Outline each blood parasite and name the species.
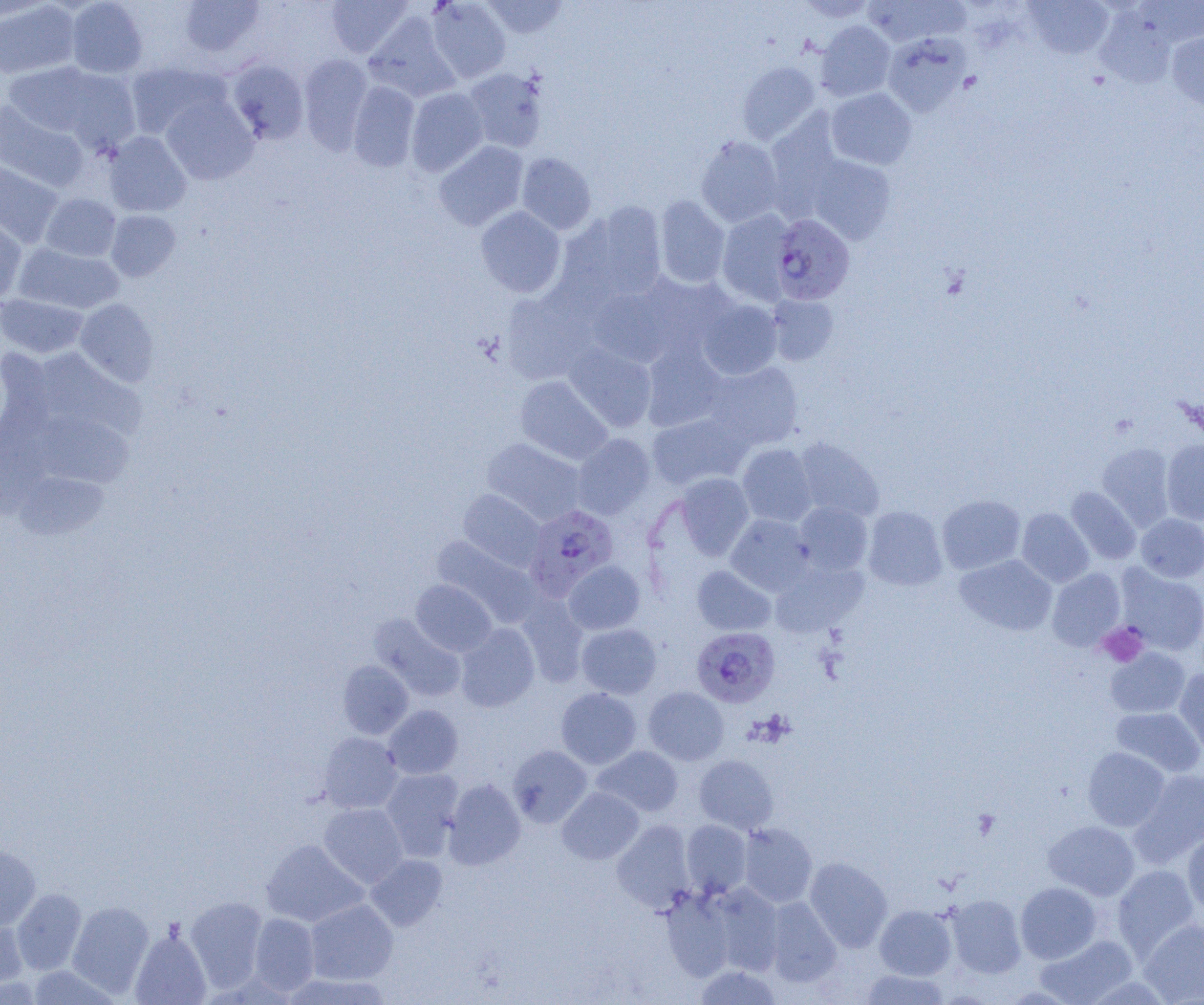
Approximate bounding boxes as (x1, y1, x2, y2) in pixels.
Plasmodium falciparum-infected red blood cells: (771, 213, 855, 304), (524, 504, 619, 600), (691, 627, 780, 708).
No Plasmodium ovale, Plasmodium malariae, Plasmodium vivax, Babesia divergens, or Trypanosoma brucei observed.

Summary:
  - Uninfected red blood cell locations: (0, 0, 52, 23), (65, 0, 148, 78), (178, 0, 267, 59), (326, 0, 412, 58), (426, 0, 511, 83), (481, 0, 569, 39), (796, 0, 877, 22), (862, 0, 971, 46), (1137, 0, 1204, 48), (0, 1, 81, 80), (1023, 1, 1114, 60), (1093, 7, 1178, 88), (364, 12, 461, 102), (815, 21, 896, 101), (883, 32, 971, 116), (1166, 32, 1204, 111), (298, 54, 373, 153), (225, 58, 309, 144), (2, 61, 111, 139), (737, 61, 820, 144), (125, 62, 227, 139), (52, 67, 142, 153), (463, 68, 548, 153), (347, 81, 420, 172), (406, 87, 488, 175), (826, 88, 917, 169), (160, 95, 258, 185), (0, 101, 88, 192), (765, 113, 844, 216), (103, 131, 191, 217), (695, 135, 783, 227), (433, 141, 528, 231), (516, 152, 596, 235), (805, 153, 896, 244), (0, 159, 64, 247), (40, 193, 121, 262), (654, 195, 731, 288), (572, 202, 667, 303), (475, 207, 566, 297), (717, 209, 795, 305), (105, 210, 181, 281), (0, 215, 27, 303), (14, 243, 124, 314), (636, 272, 738, 359), (586, 281, 682, 368), (501, 287, 599, 385), (0, 294, 88, 358), (767, 294, 839, 366), (697, 298, 783, 380), (75, 299, 159, 387), (564, 343, 657, 431), (640, 344, 728, 432), (0, 348, 56, 443), (36, 349, 145, 439), (703, 361, 803, 450), (515, 375, 612, 465), (31, 410, 133, 488), (647, 410, 751, 491), (572, 433, 655, 520), (481, 437, 586, 525), (794, 438, 885, 521), (1161, 439, 1204, 525), (737, 443, 817, 527), (1097, 443, 1175, 530), (14, 472, 109, 539), (675, 473, 754, 560), (1066, 487, 1141, 564), (458, 489, 546, 572), (936, 494, 1026, 574), (794, 501, 873, 575), (863, 505, 947, 591), (1017, 508, 1094, 587), (1136, 513, 1204, 583), (726, 514, 815, 595), (431, 536, 539, 626), (954, 554, 1057, 636), (563, 560, 645, 635), (769, 560, 867, 637), (1115, 564, 1204, 655), (692, 565, 776, 636), (1047, 568, 1126, 650), (411, 580, 497, 656), (516, 594, 589, 687), (369, 614, 466, 701), (455, 623, 539, 712), (576, 623, 662, 699), (1105, 647, 1190, 718), (337, 660, 414, 740), (1175, 667, 1204, 755), (643, 686, 729, 765), (556, 687, 642, 768), (384, 705, 463, 779), (1111, 707, 1204, 778), (318, 732, 404, 814), (508, 745, 592, 828), (592, 745, 683, 817), (1082, 747, 1170, 831), (694, 755, 778, 834), (380, 768, 464, 860), (1131, 769, 1204, 866), (443, 778, 526, 870), (557, 787, 644, 864), (319, 802, 408, 887), (681, 819, 752, 897), (612, 820, 695, 912), (1043, 820, 1139, 900), (738, 823, 817, 908), (1182, 833, 1204, 915), (261, 839, 368, 927), (0, 845, 40, 930), (366, 854, 447, 931), (805, 857, 892, 952), (1112, 865, 1201, 961), (1015, 882, 1101, 963), (708, 884, 784, 975), (661, 885, 740, 980), (12, 888, 87, 975), (945, 894, 1027, 979), (184, 896, 268, 991), (764, 897, 842, 988), (305, 899, 397, 984), (68, 901, 154, 997), (875, 905, 957, 980), (249, 913, 320, 996), (0, 918, 29, 990), (1138, 919, 1204, 1004), (130, 928, 210, 1005), (1035, 934, 1137, 1004), (25, 965, 122, 1004), (694, 965, 782, 1005), (860, 969, 950, 1004), (283, 973, 392, 1004)
  - Platelet locations: (1097, 623, 1148, 667)
  - Slide-level diagnosis: Plasmodium falciparum
  - Field of view: single
  - Magnification: 1000x
  - Image size: 1204×1005 pixels
  - Preparation: thin blood smear
  - Modality: light microscopy